Locate and identify every blood parasite.
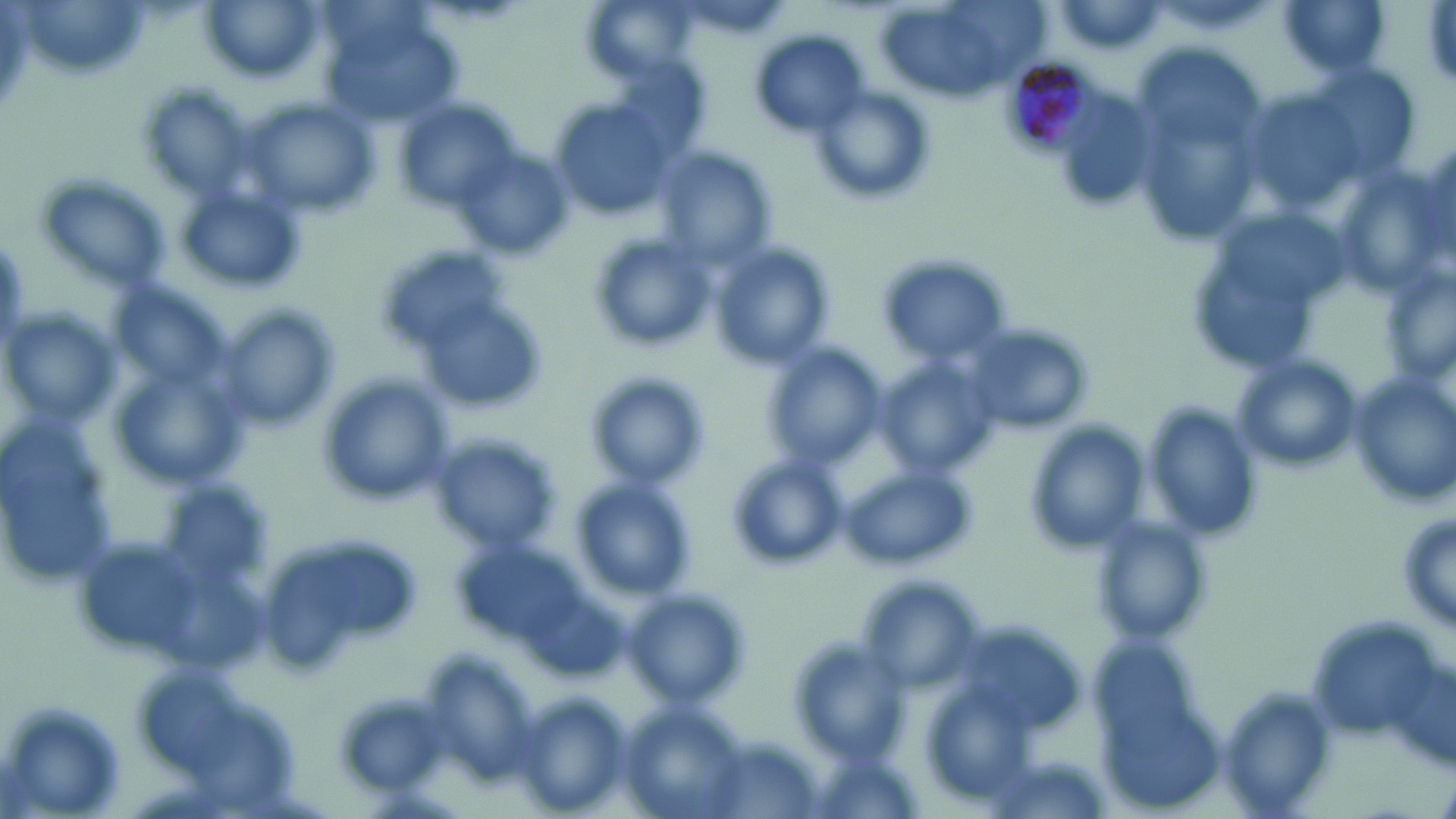

Approximate bounding boxes as (x1,y1)-(x2,y2) corner pairs in pixels.
Plasmodium malariae-infected red blood cells: (998,53)-(1107,158).
No Plasmodium falciparum, Plasmodium ovale, Plasmodium vivax, Babesia divergens, or Trypanosoma brucei observed.

Summary:
  - Uninfected red blood cell locations: (199,0)-(325,83), (1277,0)-(1392,79), (876,1)-(1033,105), (1051,2)-(1171,56), (324,18)-(462,126), (752,29)-(870,138), (1122,41)-(1268,242), (805,85)-(936,208), (396,98)-(527,216), (547,100)-(677,220), (242,101)-(378,222), (652,144)-(778,268), (454,145)-(570,261), (31,173)-(175,297), (176,182)-(308,295), (588,234)-(717,354), (711,246)-(832,369), (876,255)-(1016,367), (222,309)-(337,431), (3,312)-(121,424), (960,323)-(1093,435), (767,347)-(886,469), (1233,356)-(1362,477), (880,362)-(999,477), (1353,371)-(1453,503), (583,372)-(711,493), (320,374)-(454,506), (1143,403)-(1262,543), (1026,423)-(1146,557), (427,431)-(563,555), (0,433)-(121,586), (728,454)-(844,568), (841,466)-(975,568), (572,480)-(698,601), (1397,508)-(1455,638), (1091,518)-(1215,647), (260,533)-(426,671), (620,590)-(750,711), (789,638)-(911,767), (1216,686)-(1338,819), (513,693)-(631,818), (0,700)-(128,817), (619,706)-(752,819)
  - Slide-level diagnosis: Plasmodium malariae
  - Stain: May-Grünwald-Giemsa
  - Preparation: thin blood film
  - Magnification: 1000x
  - Modality: light microscopy
  - Image size: 1456×819 pixels
  - Field of view: single